Point out each Plasmodium parasite.
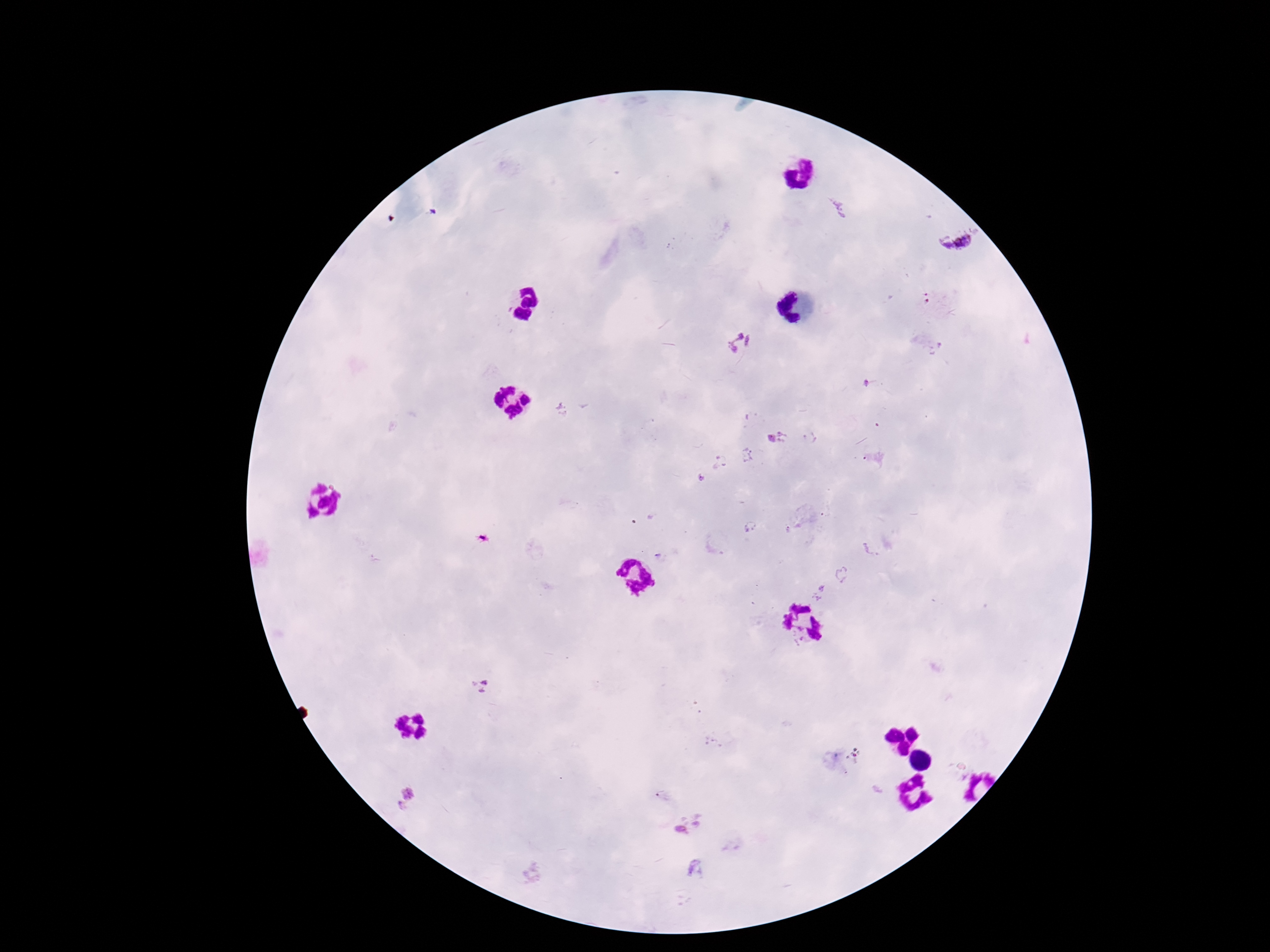

Approximate centers as [x, y] in pixels.
Plasmodium parasites: [838, 207], [956, 242], [741, 343], [778, 438], [703, 478], [480, 687], [407, 797], [690, 827], [697, 868].

Thick blood smear. 100x magnification. Photographed through the microscope eyepiece with a smartphone camera. Patient malaria status: infected. Image is 1270×952 pixels. Single field of view. Giemsa stain.